Report the malaria status of this cell.
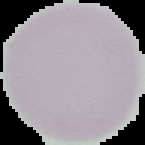
It is uninfected.

image size = 145×145 pixels
image type = segmented cell region with the area outside set to black
preparation = thin blood film